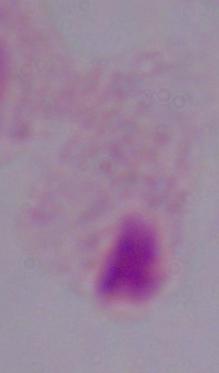
identification: trichomonad
magnification: 1000x
modality: photomicrograph